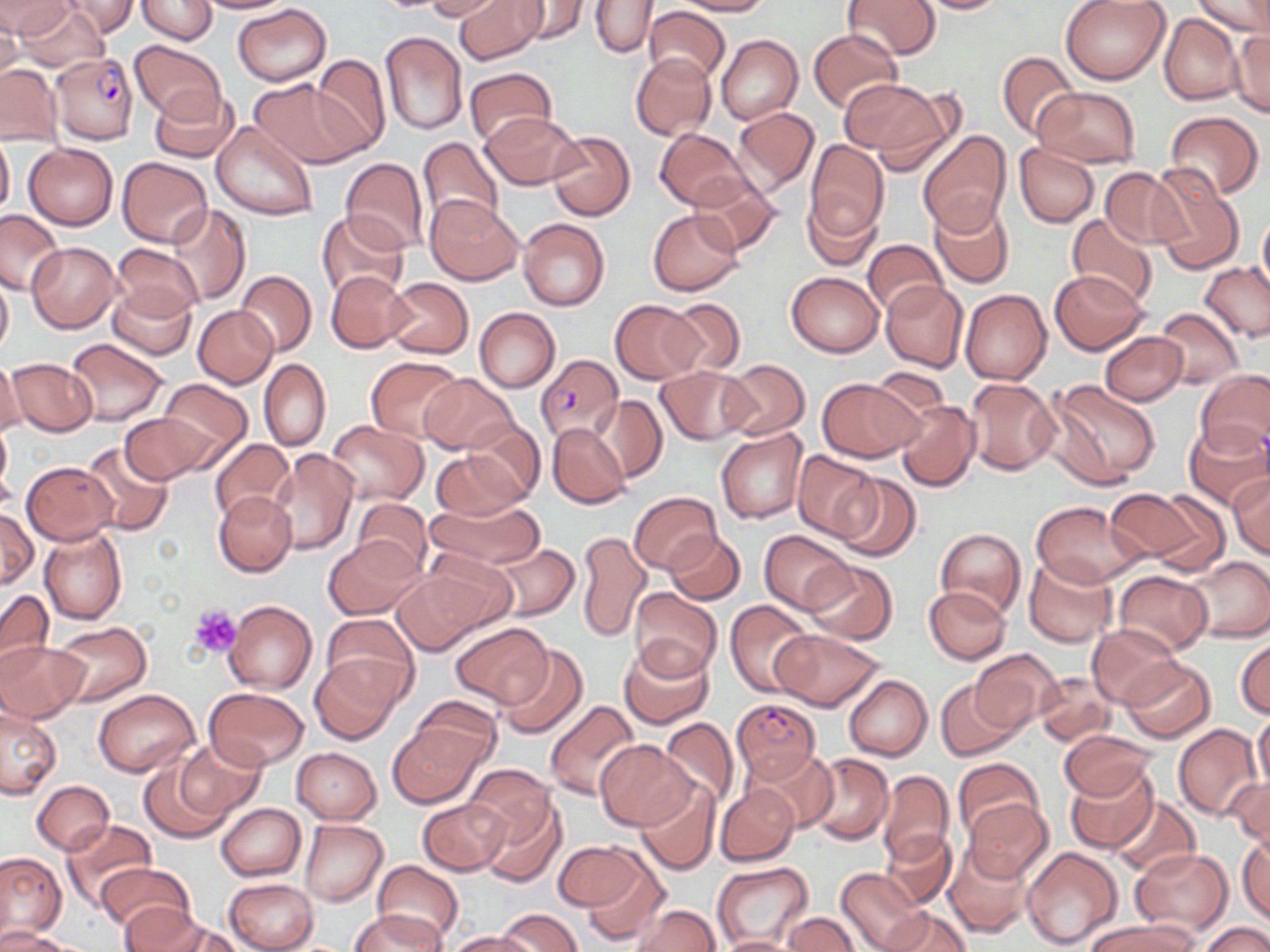

Summary:
  - Coordinate format: approximate bounding boxes as named x1/y1/x2/y2 corners in pixels
  - Plasmodium falciparum-infected red blood cell locations: (x1=53, y1=51, x2=139, y2=143), (x1=534, y1=354, x2=623, y2=445), (x1=731, y1=697, x2=821, y2=784)
  - Platelet locations: (x1=191, y1=603, x2=243, y2=659)
  - Uninfected red blood cell locations: (x1=0, y1=0, x2=75, y2=40), (x1=60, y1=0, x2=137, y2=38), (x1=136, y1=0, x2=217, y2=44), (x1=193, y1=0, x2=295, y2=14), (x1=423, y1=0, x2=508, y2=22), (x1=454, y1=0, x2=545, y2=64), (x1=506, y1=0, x2=591, y2=45), (x1=672, y1=0, x2=772, y2=15), (x1=906, y1=0, x2=1014, y2=15), (x1=1059, y1=0, x2=1171, y2=85), (x1=1192, y1=0, x2=1269, y2=41), (x1=591, y1=1, x2=659, y2=58), (x1=843, y1=1, x2=940, y2=61), (x1=12, y1=2, x2=108, y2=72), (x1=232, y1=3, x2=331, y2=85), (x1=643, y1=5, x2=730, y2=87), (x1=0, y1=8, x2=23, y2=81), (x1=1159, y1=12, x2=1244, y2=105), (x1=807, y1=28, x2=903, y2=114), (x1=1229, y1=30, x2=1269, y2=119), (x1=379, y1=31, x2=468, y2=136), (x1=716, y1=34, x2=802, y2=125), (x1=129, y1=40, x2=225, y2=123), (x1=996, y1=51, x2=1080, y2=139), (x1=310, y1=53, x2=391, y2=153), (x1=631, y1=53, x2=716, y2=141), (x1=0, y1=63, x2=63, y2=144), (x1=464, y1=67, x2=554, y2=146), (x1=249, y1=78, x2=366, y2=169), (x1=839, y1=78, x2=943, y2=158), (x1=148, y1=87, x2=240, y2=164), (x1=1032, y1=87, x2=1140, y2=165), (x1=732, y1=105, x2=820, y2=197), (x1=481, y1=111, x2=582, y2=191), (x1=1163, y1=111, x2=1264, y2=199), (x1=211, y1=120, x2=318, y2=222), (x1=655, y1=128, x2=752, y2=212), (x1=547, y1=129, x2=635, y2=221), (x1=918, y1=130, x2=1011, y2=235), (x1=0, y1=133, x2=14, y2=217), (x1=417, y1=136, x2=503, y2=233), (x1=804, y1=140, x2=888, y2=245), (x1=23, y1=143, x2=118, y2=229), (x1=1013, y1=145, x2=1099, y2=227), (x1=117, y1=156, x2=212, y2=248), (x1=340, y1=157, x2=429, y2=254), (x1=1147, y1=164, x2=1244, y2=273), (x1=1100, y1=168, x2=1185, y2=249), (x1=688, y1=173, x2=780, y2=255), (x1=801, y1=192, x2=881, y2=269), (x1=426, y1=197, x2=522, y2=284), (x1=928, y1=200, x2=1014, y2=288), (x1=164, y1=203, x2=249, y2=306), (x1=0, y1=208, x2=65, y2=295), (x1=648, y1=209, x2=743, y2=295), (x1=316, y1=210, x2=410, y2=300), (x1=1257, y1=212, x2=1270, y2=299), (x1=1066, y1=214, x2=1158, y2=310), (x1=517, y1=216, x2=610, y2=311), (x1=863, y1=238, x2=948, y2=318), (x1=27, y1=242, x2=120, y2=331), (x1=112, y1=243, x2=203, y2=320), (x1=1199, y1=263, x2=1270, y2=342), (x1=235, y1=270, x2=316, y2=357), (x1=326, y1=270, x2=413, y2=353), (x1=1050, y1=270, x2=1149, y2=355), (x1=786, y1=271, x2=883, y2=356), (x1=0, y1=274, x2=13, y2=360), (x1=384, y1=276, x2=474, y2=358), (x1=880, y1=281, x2=968, y2=372), (x1=107, y1=282, x2=197, y2=360), (x1=960, y1=289, x2=1051, y2=385), (x1=664, y1=296, x2=746, y2=376), (x1=610, y1=299, x2=704, y2=385), (x1=193, y1=305, x2=278, y2=388), (x1=474, y1=307, x2=559, y2=393), (x1=1153, y1=308, x2=1244, y2=388), (x1=1100, y1=332, x2=1188, y2=405), (x1=65, y1=337, x2=168, y2=426), (x1=366, y1=356, x2=464, y2=442), (x1=6, y1=357, x2=96, y2=437), (x1=0, y1=358, x2=25, y2=439), (x1=259, y1=358, x2=331, y2=452), (x1=719, y1=359, x2=809, y2=440), (x1=656, y1=366, x2=755, y2=445), (x1=1195, y1=368, x2=1270, y2=460), (x1=419, y1=374, x2=519, y2=454), (x1=817, y1=377, x2=922, y2=462), (x1=965, y1=377, x2=1060, y2=476), (x1=1046, y1=378, x2=1160, y2=486), (x1=158, y1=379, x2=252, y2=463), (x1=592, y1=395, x2=668, y2=483), (x1=895, y1=398, x2=979, y2=491), (x1=120, y1=411, x2=214, y2=483), (x1=0, y1=417, x2=13, y2=508), (x1=324, y1=419, x2=429, y2=506), (x1=462, y1=419, x2=546, y2=503), (x1=1183, y1=420, x2=1270, y2=510), (x1=547, y1=423, x2=629, y2=510), (x1=715, y1=426, x2=807, y2=523), (x1=210, y1=439, x2=296, y2=523), (x1=80, y1=441, x2=173, y2=536), (x1=266, y1=449, x2=358, y2=555), (x1=429, y1=449, x2=529, y2=521), (x1=794, y1=451, x2=879, y2=541), (x1=22, y1=462, x2=118, y2=544), (x1=831, y1=473, x2=920, y2=562), (x1=1229, y1=473, x2=1270, y2=559), (x1=1111, y1=487, x2=1219, y2=570), (x1=628, y1=491, x2=722, y2=575), (x1=214, y1=492, x2=297, y2=578), (x1=1147, y1=495, x2=1247, y2=605), (x1=350, y1=498, x2=433, y2=577), (x1=425, y1=498, x2=545, y2=572), (x1=1032, y1=501, x2=1148, y2=589), (x1=0, y1=509, x2=38, y2=588), (x1=38, y1=526, x2=128, y2=625), (x1=936, y1=528, x2=1026, y2=620), (x1=760, y1=529, x2=854, y2=612), (x1=575, y1=530, x2=652, y2=642), (x1=664, y1=531, x2=745, y2=605), (x1=323, y1=536, x2=425, y2=621), (x1=485, y1=542, x2=580, y2=621), (x1=421, y1=549, x2=519, y2=632), (x1=1023, y1=556, x2=1117, y2=648), (x1=1182, y1=556, x2=1270, y2=643), (x1=803, y1=560, x2=899, y2=645), (x1=391, y1=564, x2=501, y2=654), (x1=1113, y1=571, x2=1213, y2=656), (x1=924, y1=586, x2=1010, y2=664), (x1=629, y1=588, x2=721, y2=679), (x1=0, y1=589, x2=53, y2=679), (x1=725, y1=599, x2=814, y2=696), (x1=224, y1=600, x2=317, y2=694), (x1=321, y1=613, x2=417, y2=701), (x1=52, y1=622, x2=152, y2=706), (x1=451, y1=624, x2=551, y2=706), (x1=1086, y1=625, x2=1182, y2=707), (x1=771, y1=627, x2=885, y2=711), (x1=1236, y1=636, x2=1269, y2=720), (x1=0, y1=639, x2=88, y2=723), (x1=619, y1=641, x2=714, y2=729), (x1=493, y1=644, x2=588, y2=740), (x1=969, y1=649, x2=1064, y2=735), (x1=310, y1=655, x2=402, y2=743), (x1=1119, y1=658, x2=1217, y2=743), (x1=1035, y1=671, x2=1116, y2=746), (x1=843, y1=675, x2=932, y2=761), (x1=935, y1=680, x2=1022, y2=761), (x1=93, y1=688, x2=200, y2=776), (x1=204, y1=688, x2=308, y2=770), (x1=407, y1=697, x2=500, y2=778), (x1=544, y1=700, x2=642, y2=802), (x1=0, y1=705, x2=62, y2=798), (x1=1252, y1=709, x2=1270, y2=801), (x1=659, y1=718, x2=741, y2=807), (x1=388, y1=722, x2=486, y2=807), (x1=1172, y1=724, x2=1262, y2=821), (x1=1057, y1=728, x2=1158, y2=802), (x1=174, y1=739, x2=265, y2=822), (x1=594, y1=739, x2=695, y2=830), (x1=292, y1=747, x2=381, y2=823), (x1=743, y1=747, x2=837, y2=833), (x1=802, y1=753, x2=894, y2=845), (x1=953, y1=756, x2=1042, y2=841), (x1=139, y1=759, x2=231, y2=843), (x1=1065, y1=764, x2=1157, y2=853), (x1=465, y1=765, x2=558, y2=850), (x1=876, y1=770, x2=955, y2=868), (x1=1226, y1=774, x2=1270, y2=850), (x1=635, y1=777, x2=719, y2=875), (x1=31, y1=779, x2=114, y2=855), (x1=716, y1=783, x2=800, y2=866), (x1=475, y1=792, x2=565, y2=886), (x1=1108, y1=797, x2=1199, y2=878), (x1=418, y1=798, x2=509, y2=875), (x1=964, y1=798, x2=1054, y2=883), (x1=216, y1=803, x2=305, y2=880), (x1=60, y1=818, x2=155, y2=910), (x1=300, y1=818, x2=388, y2=905), (x1=881, y1=829, x2=958, y2=911), (x1=1237, y1=831, x2=1269, y2=925), (x1=553, y1=840, x2=642, y2=912), (x1=944, y1=843, x2=1033, y2=937), (x1=579, y1=846, x2=670, y2=947), (x1=1021, y1=846, x2=1124, y2=950), (x1=1129, y1=847, x2=1234, y2=938), (x1=0, y1=850, x2=66, y2=940), (x1=96, y1=861, x2=196, y2=935), (x1=373, y1=861, x2=464, y2=946), (x1=712, y1=863, x2=814, y2=948), (x1=835, y1=868, x2=927, y2=952), (x1=224, y1=878, x2=318, y2=952), (x1=121, y1=904, x2=217, y2=952), (x1=631, y1=904, x2=720, y2=952), (x1=881, y1=906, x2=972, y2=952), (x1=496, y1=907, x2=583, y2=952), (x1=353, y1=909, x2=446, y2=952), (x1=783, y1=913, x2=861, y2=952), (x1=1085, y1=920, x2=1198, y2=952), (x1=1199, y1=922, x2=1270, y2=952), (x1=0, y1=929, x2=79, y2=952), (x1=447, y1=931, x2=536, y2=952), (x1=709, y1=935, x2=806, y2=952)
  - Slide-level diagnosis: Plasmodium falciparum
  - Magnification: 1000x
  - Stain: May-Grünwald-Giemsa
  - Preparation: thin blood smear
  - Field of view: single
  - Image size: 1270×952 pixels
  - Modality: light microscopy